Give the position of every Plasmodium parasite visible.
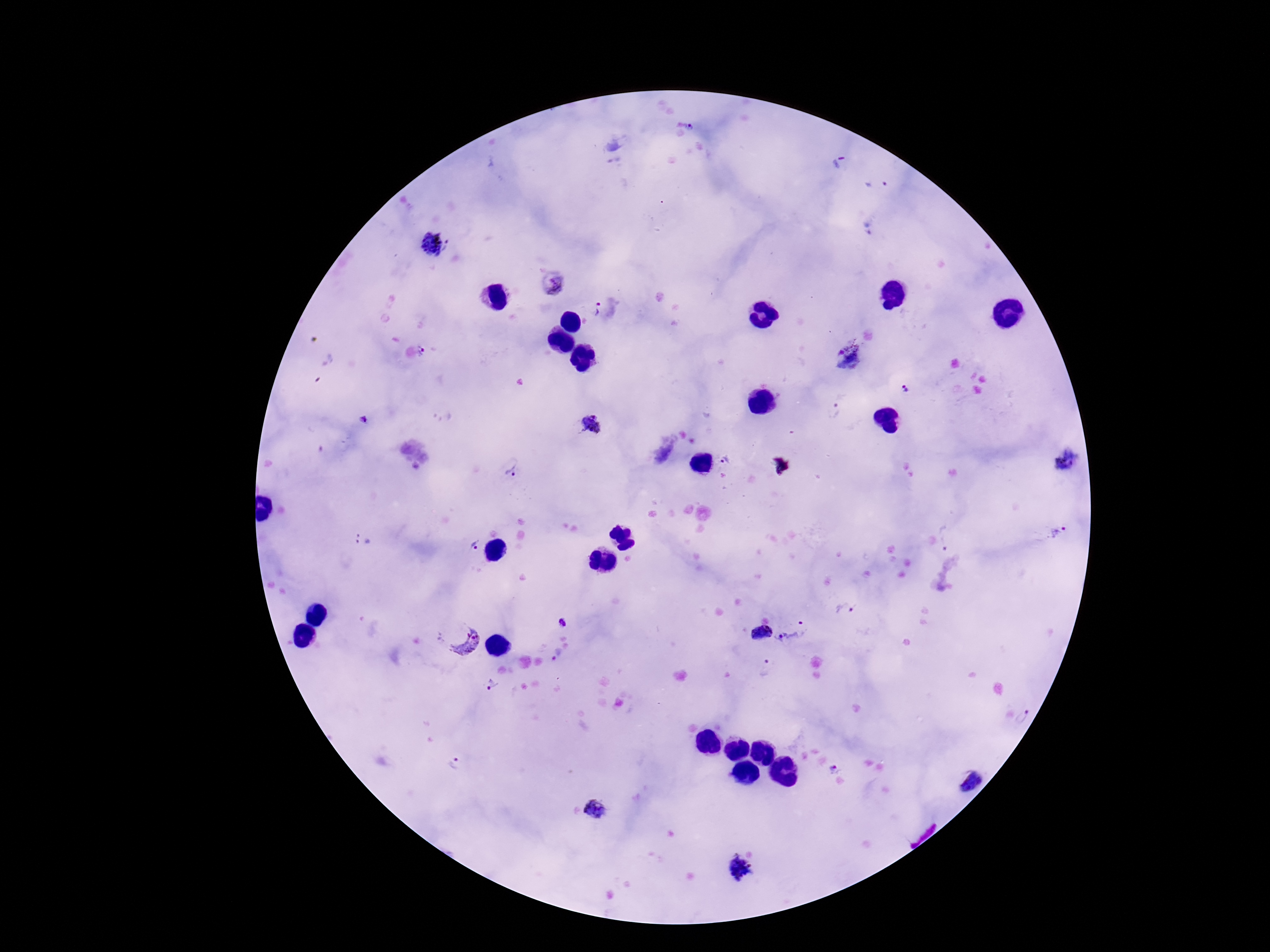
Approximate centers as [x, y] in pixels.
Plasmodium parasites: [691, 128], [430, 244], [449, 246], [553, 285], [596, 309], [422, 351], [850, 356], [906, 390], [834, 409], [363, 420], [591, 424], [726, 461], [1066, 461], [512, 472], [1057, 533], [946, 538], [364, 539], [473, 546], [844, 610], [802, 622], [563, 623], [762, 634], [461, 638], [792, 639], [765, 670], [491, 684], [1024, 718], [457, 765], [834, 768], [967, 780], [594, 809], [740, 869].

Summary:
  - Image size: 1270×952 pixels
  - Capture: smartphone camera through the microscope eyepiece
  - Magnification: 100x
  - Preparation: thick blood film
  - Stain: Giemsa
  - Patient malaria status: infected
  - Field of view: single